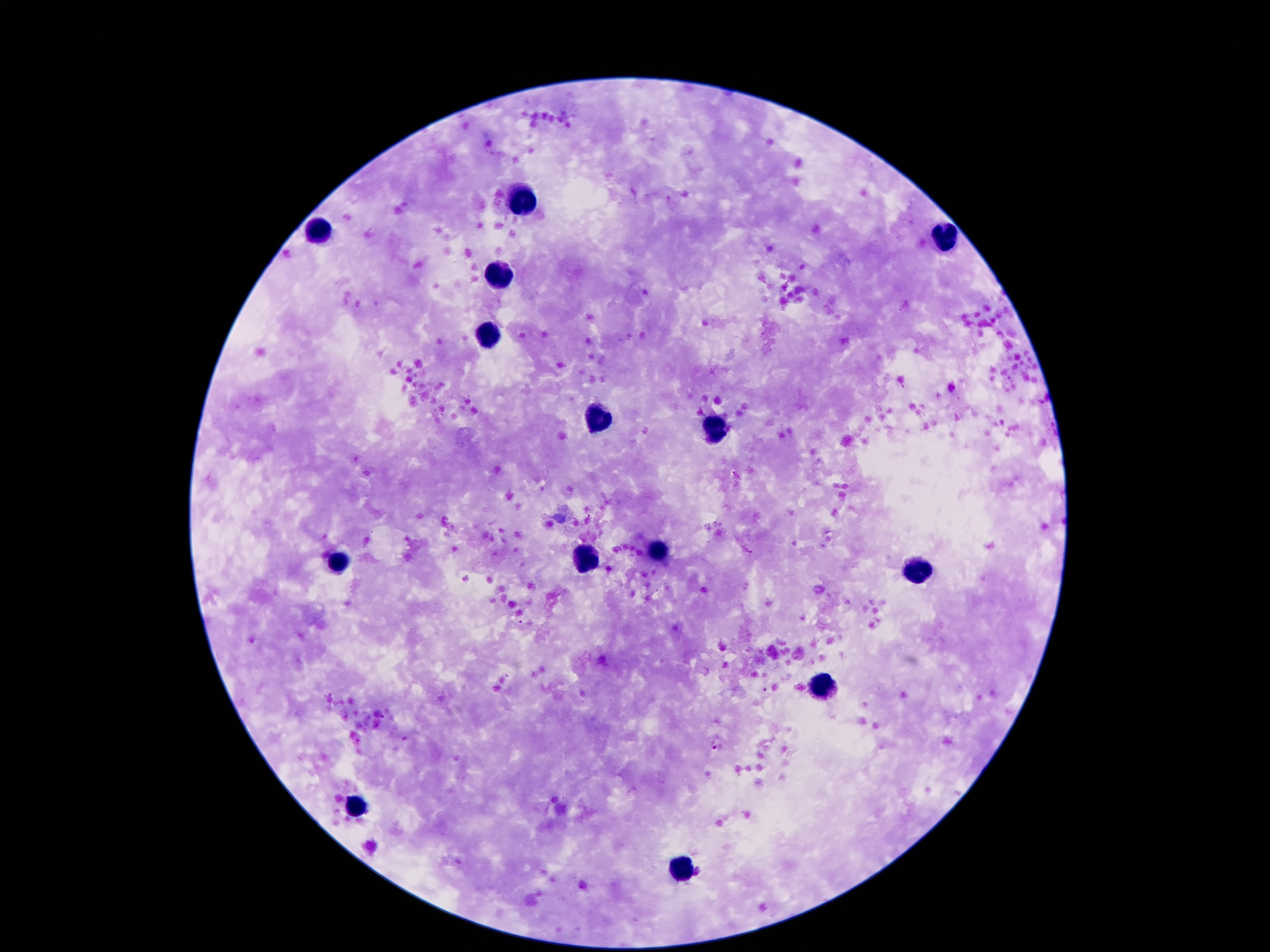
Approximate centers as (x, y) in pixels. Leukocyte locations: (521, 198), (320, 228), (939, 238), (504, 276), (486, 333), (601, 417), (716, 427), (658, 552), (586, 561), (337, 564), (920, 571), (824, 685), (355, 808), (681, 871). Single field of view. Thick peripheral-blood smear. Image is 1270×952 pixels. Giemsa-stained preparation. Patient malaria status: uninfected. Photographed through the microscope eyepiece with a smartphone camera. 100x magnification.